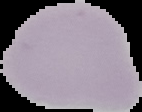

Summary:
  - Result: no Plasmodium parasites detected
  - Image type: segmented cell region with the area outside set to black
  - Preparation: thin blood smear
  - Image size: 142×112 pixels